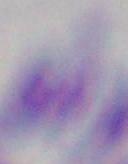

Summary:
  - Identification: Toxoplasma gondii
  - Magnification: 1000x
  - Modality: photomicrograph